Assess this cell for malaria.
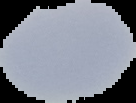

It is uninfected.

{
  "image_type": "cell region segmented out of the field of view; surrounding area masked to black",
  "preparation": "thin blood film",
  "image_size": "136×103 pixels"
}